Outline each Plasmodium falciparum-infected red blood cell.
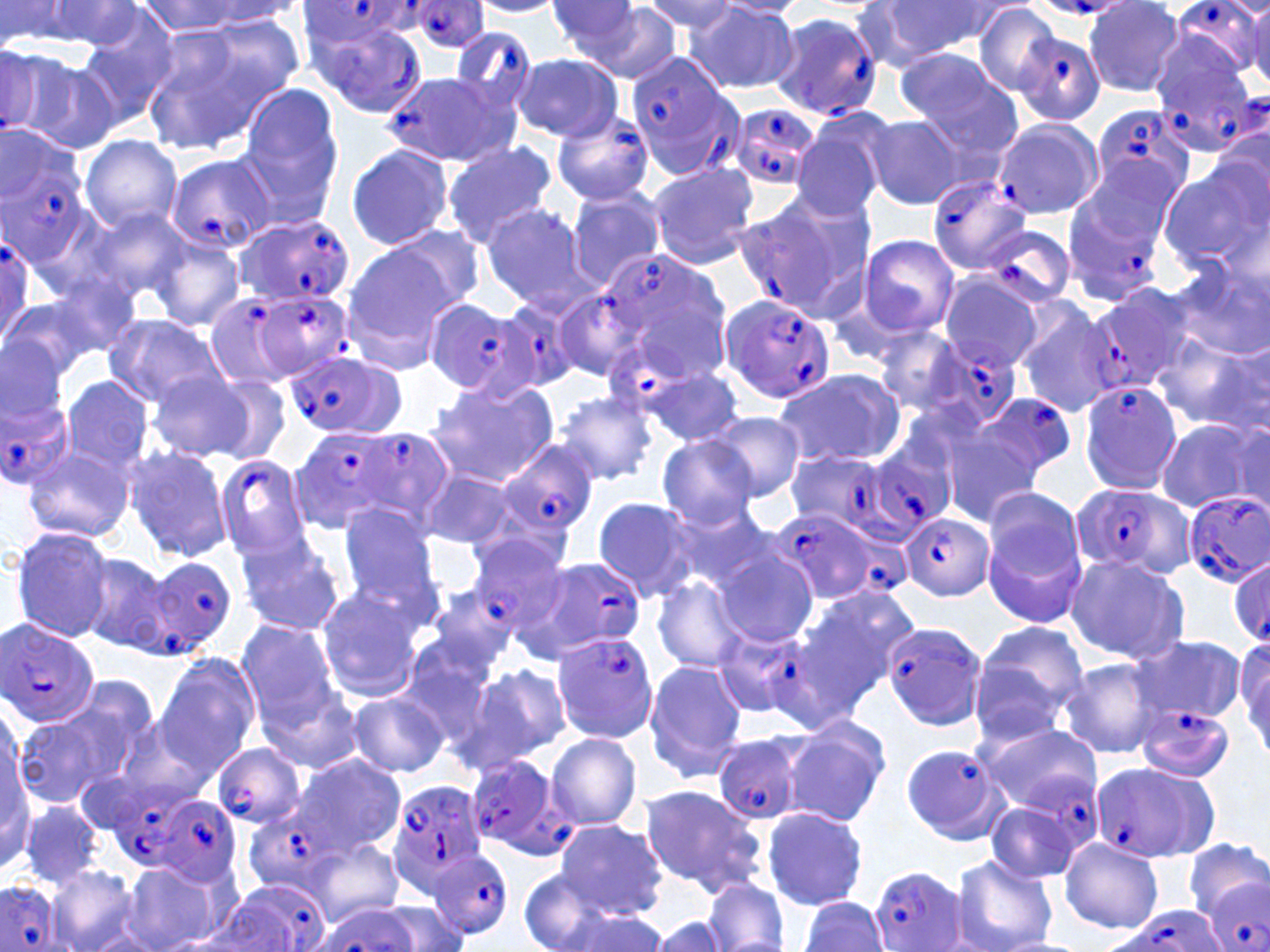
Approximate bounding boxes as named x1/y1/x2/y2 corners in pixels.
Plasmodium falciparum-infected red blood cells: (x1=1170, y1=0, x2=1265, y2=77), (x1=410, y1=1, x2=488, y2=52), (x1=300, y1=3, x2=417, y2=49), (x1=768, y1=12, x2=884, y2=121), (x1=308, y1=16, x2=426, y2=118), (x1=1001, y1=16, x2=1103, y2=118), (x1=449, y1=26, x2=537, y2=115), (x1=1148, y1=34, x2=1256, y2=143), (x1=623, y1=50, x2=739, y2=182), (x1=386, y1=71, x2=517, y2=169), (x1=1088, y1=103, x2=1197, y2=201), (x1=727, y1=104, x2=821, y2=191), (x1=549, y1=110, x2=655, y2=207), (x1=0, y1=130, x2=97, y2=282), (x1=163, y1=153, x2=273, y2=255), (x1=925, y1=177, x2=1030, y2=275), (x1=1062, y1=185, x2=1167, y2=303), (x1=733, y1=196, x2=862, y2=318), (x1=233, y1=215, x2=356, y2=310), (x1=981, y1=224, x2=1076, y2=307), (x1=0, y1=228, x2=39, y2=348), (x1=591, y1=253, x2=736, y2=385), (x1=1086, y1=282, x2=1201, y2=392), (x1=256, y1=288, x2=357, y2=380), (x1=550, y1=289, x2=644, y2=383), (x1=202, y1=291, x2=305, y2=394), (x1=719, y1=294, x2=835, y2=403), (x1=429, y1=300, x2=530, y2=394), (x1=495, y1=301, x2=581, y2=393), (x1=604, y1=339, x2=693, y2=422), (x1=925, y1=339, x2=1024, y2=431), (x1=285, y1=352, x2=403, y2=436), (x1=1077, y1=376, x2=1185, y2=494), (x1=2, y1=383, x2=73, y2=490), (x1=971, y1=392, x2=1080, y2=485), (x1=351, y1=427, x2=451, y2=526), (x1=294, y1=429, x2=395, y2=525), (x1=847, y1=439, x2=959, y2=542), (x1=494, y1=440, x2=600, y2=542), (x1=214, y1=454, x2=312, y2=560), (x1=1071, y1=482, x2=1191, y2=580), (x1=1180, y1=491, x2=1269, y2=587), (x1=768, y1=506, x2=886, y2=605), (x1=903, y1=512, x2=994, y2=600), (x1=467, y1=537, x2=567, y2=632), (x1=144, y1=555, x2=237, y2=654), (x1=523, y1=555, x2=645, y2=657), (x1=1229, y1=557, x2=1270, y2=649), (x1=1, y1=617, x2=100, y2=727), (x1=879, y1=618, x2=989, y2=732), (x1=712, y1=625, x2=808, y2=720), (x1=550, y1=633, x2=659, y2=745), (x1=1135, y1=704, x2=1234, y2=784), (x1=713, y1=734, x2=805, y2=826), (x1=212, y1=743, x2=306, y2=827), (x1=898, y1=744, x2=1009, y2=844), (x1=461, y1=757, x2=575, y2=859), (x1=1091, y1=761, x2=1217, y2=866), (x1=1020, y1=769, x2=1102, y2=853), (x1=111, y1=783, x2=213, y2=867), (x1=389, y1=783, x2=488, y2=883), (x1=156, y1=796, x2=243, y2=886), (x1=244, y1=806, x2=343, y2=895), (x1=429, y1=847, x2=515, y2=940), (x1=870, y1=865, x2=968, y2=951), (x1=1197, y1=873, x2=1270, y2=952), (x1=0, y1=880, x2=60, y2=952), (x1=223, y1=880, x2=331, y2=951), (x1=1107, y1=907, x2=1227, y2=952).

{
  "slide_level_diagnosis": "Plasmodium falciparum",
  "magnification": "1000x",
  "image_size": "1270×952 pixels",
  "stain": "May-Grünwald-Giemsa",
  "uninfected_red_blood_cell_locations": "approximate bounding boxes as named x1/y1/x2/y2 corners in pixels: (x1=544, y1=0, x2=653, y2=67), (x1=639, y1=0, x2=739, y2=37), (x1=0, y1=1, x2=94, y2=49), (x1=30, y1=1, x2=147, y2=50), (x1=137, y1=1, x2=254, y2=38), (x1=468, y1=1, x2=567, y2=17), (x1=880, y1=1, x2=1010, y2=59), (x1=190, y1=2, x2=307, y2=26), (x1=715, y1=2, x2=807, y2=20), (x1=1083, y1=2, x2=1186, y2=97), (x1=584, y1=4, x2=684, y2=82), (x1=683, y1=4, x2=800, y2=93), (x1=974, y1=4, x2=1063, y2=94), (x1=1246, y1=5, x2=1270, y2=89), (x1=203, y1=11, x2=309, y2=100), (x1=76, y1=13, x2=178, y2=126), (x1=138, y1=24, x2=283, y2=154), (x1=0, y1=45, x2=71, y2=143), (x1=20, y1=53, x2=123, y2=155), (x1=894, y1=53, x2=1021, y2=156), (x1=512, y1=54, x2=623, y2=141), (x1=242, y1=87, x2=342, y2=185), (x1=865, y1=114, x2=965, y2=209), (x1=789, y1=116, x2=891, y2=221), (x1=233, y1=117, x2=345, y2=232), (x1=991, y1=118, x2=1104, y2=220), (x1=79, y1=134, x2=182, y2=234), (x1=441, y1=141, x2=557, y2=248), (x1=344, y1=143, x2=454, y2=252), (x1=1071, y1=153, x2=1185, y2=259), (x1=646, y1=162, x2=759, y2=269), (x1=1158, y1=162, x2=1267, y2=271), (x1=566, y1=189, x2=666, y2=291), (x1=481, y1=203, x2=592, y2=309), (x1=81, y1=206, x2=194, y2=304), (x1=387, y1=225, x2=485, y2=311), (x1=859, y1=235, x2=958, y2=335), (x1=151, y1=238, x2=245, y2=330), (x1=343, y1=246, x2=458, y2=363), (x1=1169, y1=263, x2=1267, y2=359), (x1=940, y1=271, x2=1047, y2=373), (x1=2, y1=294, x2=100, y2=389), (x1=1016, y1=305, x2=1119, y2=417), (x1=104, y1=314, x2=228, y2=406), (x1=877, y1=326, x2=967, y2=415), (x1=1161, y1=333, x2=1268, y2=432), (x1=0, y1=335, x2=71, y2=443), (x1=655, y1=366, x2=740, y2=446), (x1=146, y1=369, x2=254, y2=462), (x1=773, y1=369, x2=904, y2=468), (x1=199, y1=372, x2=291, y2=463), (x1=59, y1=375, x2=155, y2=477), (x1=428, y1=377, x2=557, y2=486), (x1=556, y1=392, x2=658, y2=485), (x1=711, y1=413, x2=804, y2=501), (x1=1156, y1=420, x2=1266, y2=514), (x1=938, y1=423, x2=1052, y2=522), (x1=655, y1=435, x2=759, y2=530), (x1=24, y1=446, x2=135, y2=544), (x1=124, y1=448, x2=231, y2=560), (x1=786, y1=448, x2=857, y2=533), (x1=421, y1=470, x2=519, y2=550), (x1=983, y1=492, x2=1090, y2=633), (x1=591, y1=495, x2=699, y2=603), (x1=335, y1=502, x2=443, y2=612), (x1=665, y1=503, x2=769, y2=593), (x1=10, y1=527, x2=117, y2=644), (x1=234, y1=533, x2=346, y2=637), (x1=715, y1=548, x2=819, y2=647), (x1=76, y1=552, x2=174, y2=653), (x1=1065, y1=552, x2=1190, y2=665), (x1=653, y1=575, x2=751, y2=675), (x1=810, y1=584, x2=920, y2=683), (x1=429, y1=585, x2=521, y2=671), (x1=315, y1=588, x2=424, y2=703), (x1=776, y1=611, x2=890, y2=731), (x1=235, y1=621, x2=342, y2=725), (x1=970, y1=621, x2=1090, y2=744), (x1=1132, y1=634, x2=1246, y2=727), (x1=398, y1=635, x2=506, y2=744), (x1=1234, y1=636, x2=1269, y2=761), (x1=154, y1=656, x2=259, y2=774), (x1=1061, y1=657, x2=1165, y2=757), (x1=643, y1=660, x2=746, y2=779), (x1=466, y1=664, x2=572, y2=769), (x1=262, y1=688, x2=361, y2=774), (x1=346, y1=693, x2=448, y2=778), (x1=17, y1=699, x2=138, y2=806), (x1=117, y1=714, x2=225, y2=809), (x1=780, y1=717, x2=891, y2=828), (x1=977, y1=721, x2=1102, y2=803), (x1=544, y1=732, x2=642, y2=832), (x1=1, y1=740, x2=34, y2=874), (x1=294, y1=754, x2=406, y2=853), (x1=639, y1=785, x2=766, y2=895), (x1=21, y1=801, x2=103, y2=890), (x1=763, y1=807, x2=869, y2=911), (x1=984, y1=810, x2=1091, y2=887), (x1=554, y1=821, x2=667, y2=920), (x1=307, y1=838, x2=404, y2=924), (x1=1060, y1=839, x2=1164, y2=932), (x1=949, y1=854, x2=1058, y2=952), (x1=47, y1=864, x2=139, y2=952), (x1=121, y1=864, x2=222, y2=952), (x1=519, y1=870, x2=628, y2=952), (x1=701, y1=878, x2=787, y2=952), (x1=193, y1=897, x2=301, y2=950), (x1=801, y1=897, x2=890, y2=951), (x1=379, y1=901, x2=467, y2=952), (x1=552, y1=907, x2=673, y2=951), (x1=651, y1=916, x2=732, y2=951)",
  "preparation": "thin blood film",
  "modality": "optical microscopy",
  "field_of_view": "one of a larger specimen"
}